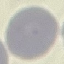

Summary:
  - Malaria status: uninfected
  - Image type: automatically extracted cell patch, resized to 64 × 64 pixels
  - Preparation: thin blood film
  - Capture: smartphone camera at the microscope eyepiece
  - Stain: Giemsa